Locate and identify every blood parasite.
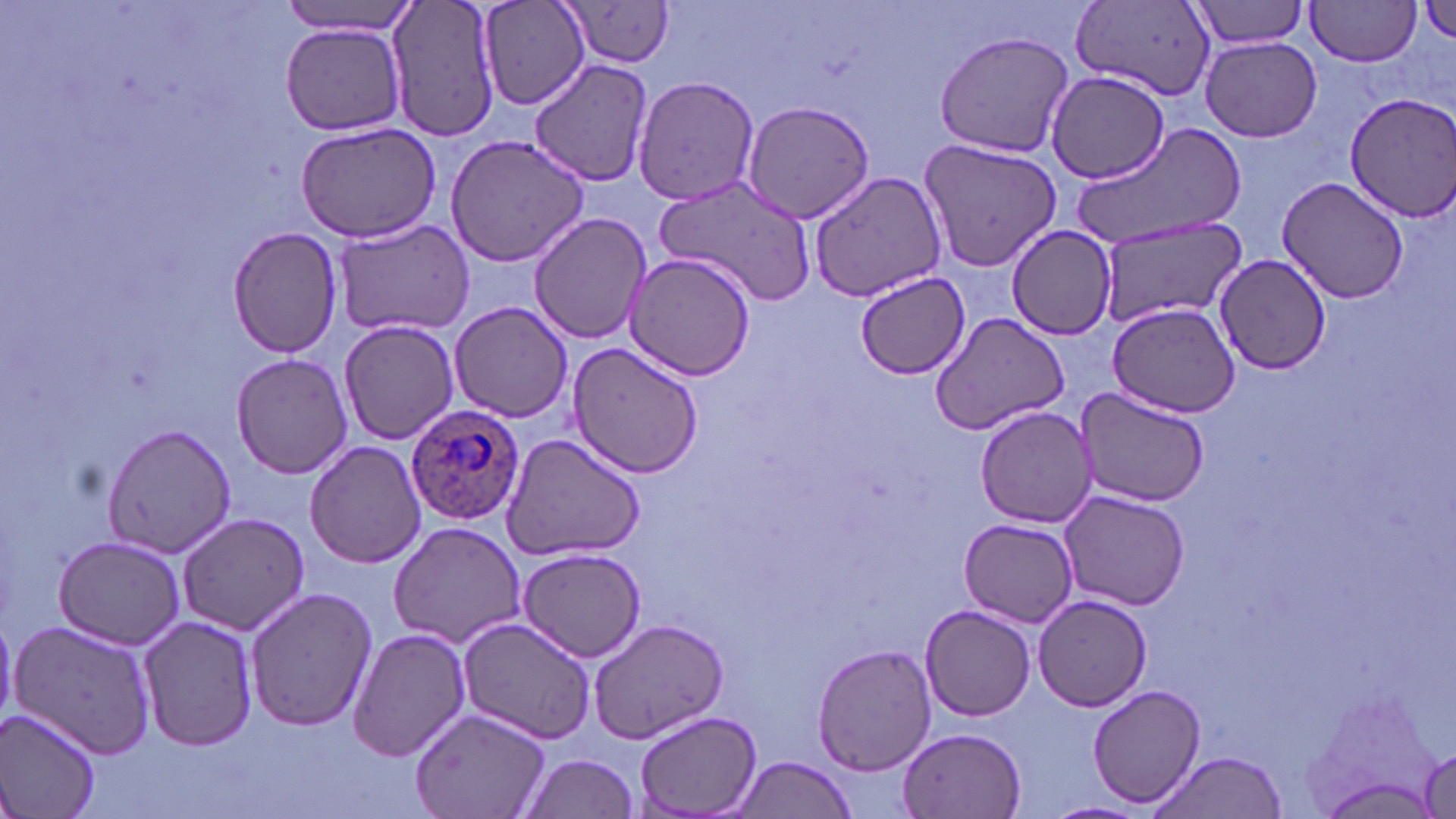

Approximate bounding boxes as named x1/y1/x2/y2 corners in pixels.
Plasmodium ovale-infected red blood cells: (x1=404, y1=403, x2=526, y2=528).
No Plasmodium falciparum, Plasmodium malariae, Plasmodium vivax, Babesia divergens, or Trypanosoma brucei observed.

{
  "slide_level_diagnosis": "Plasmodium ovale",
  "preparation": "thin blood film",
  "magnification": "1000x",
  "stain": "May-Grünwald-Giemsa",
  "image_size": "1456×819 pixels",
  "field_of_view": "one of a larger specimen",
  "uninfected_red_blood_cell_locations": "approximate bounding boxes as named x1/y1/x2/y2 corners in pixels: (x1=278, y1=0, x2=418, y2=36), (x1=385, y1=0, x2=504, y2=143), (x1=479, y1=0, x2=589, y2=111), (x1=1305, y1=0, x2=1422, y2=66), (x1=557, y1=1, x2=676, y2=72), (x1=1187, y1=1, x2=1312, y2=50), (x1=1074, y1=2, x2=1213, y2=97), (x1=1419, y1=3, x2=1456, y2=48), (x1=281, y1=23, x2=407, y2=135), (x1=933, y1=30, x2=1074, y2=159), (x1=1201, y1=36, x2=1322, y2=142), (x1=530, y1=58, x2=656, y2=185), (x1=1045, y1=72, x2=1171, y2=186), (x1=630, y1=75, x2=762, y2=207), (x1=1342, y1=92, x2=1456, y2=222), (x1=739, y1=100, x2=876, y2=224), (x1=294, y1=122, x2=441, y2=243), (x1=1074, y1=125, x2=1247, y2=251), (x1=444, y1=133, x2=591, y2=267), (x1=917, y1=135, x2=1065, y2=272), (x1=807, y1=169, x2=947, y2=301), (x1=1277, y1=175, x2=1409, y2=305), (x1=654, y1=176, x2=819, y2=303), (x1=529, y1=210, x2=653, y2=345), (x1=332, y1=218, x2=476, y2=337), (x1=1094, y1=219, x2=1247, y2=329), (x1=225, y1=226, x2=342, y2=358), (x1=1006, y1=226, x2=1119, y2=340), (x1=622, y1=251, x2=760, y2=381), (x1=1215, y1=254, x2=1332, y2=374), (x1=856, y1=271, x2=971, y2=380), (x1=450, y1=301, x2=573, y2=423), (x1=1106, y1=302, x2=1243, y2=418), (x1=929, y1=311, x2=1071, y2=435), (x1=338, y1=319, x2=458, y2=444), (x1=568, y1=341, x2=705, y2=476), (x1=230, y1=352, x2=354, y2=479), (x1=1073, y1=388, x2=1210, y2=507), (x1=975, y1=406, x2=1097, y2=527), (x1=99, y1=422, x2=238, y2=560), (x1=501, y1=432, x2=647, y2=562), (x1=306, y1=440, x2=428, y2=569), (x1=1060, y1=492, x2=1188, y2=609), (x1=178, y1=512, x2=309, y2=635), (x1=959, y1=517, x2=1079, y2=627), (x1=387, y1=521, x2=527, y2=650), (x1=52, y1=535, x2=187, y2=650), (x1=515, y1=547, x2=649, y2=662), (x1=245, y1=588, x2=377, y2=734), (x1=1032, y1=595, x2=1154, y2=712), (x1=919, y1=604, x2=1036, y2=721), (x1=138, y1=614, x2=260, y2=753), (x1=456, y1=614, x2=597, y2=746), (x1=586, y1=615, x2=730, y2=744), (x1=11, y1=620, x2=160, y2=760), (x1=347, y1=628, x2=472, y2=762), (x1=812, y1=642, x2=938, y2=776), (x1=1088, y1=683, x2=1207, y2=808), (x1=411, y1=707, x2=551, y2=819), (x1=1, y1=709, x2=104, y2=819), (x1=635, y1=710, x2=761, y2=817), (x1=896, y1=726, x2=1028, y2=818), (x1=1417, y1=741, x2=1454, y2=819), (x1=1145, y1=751, x2=1289, y2=819), (x1=518, y1=753, x2=640, y2=818), (x1=730, y1=754, x2=858, y2=819), (x1=1043, y1=799, x2=1150, y2=819)",
  "modality": "light microscopy"
}